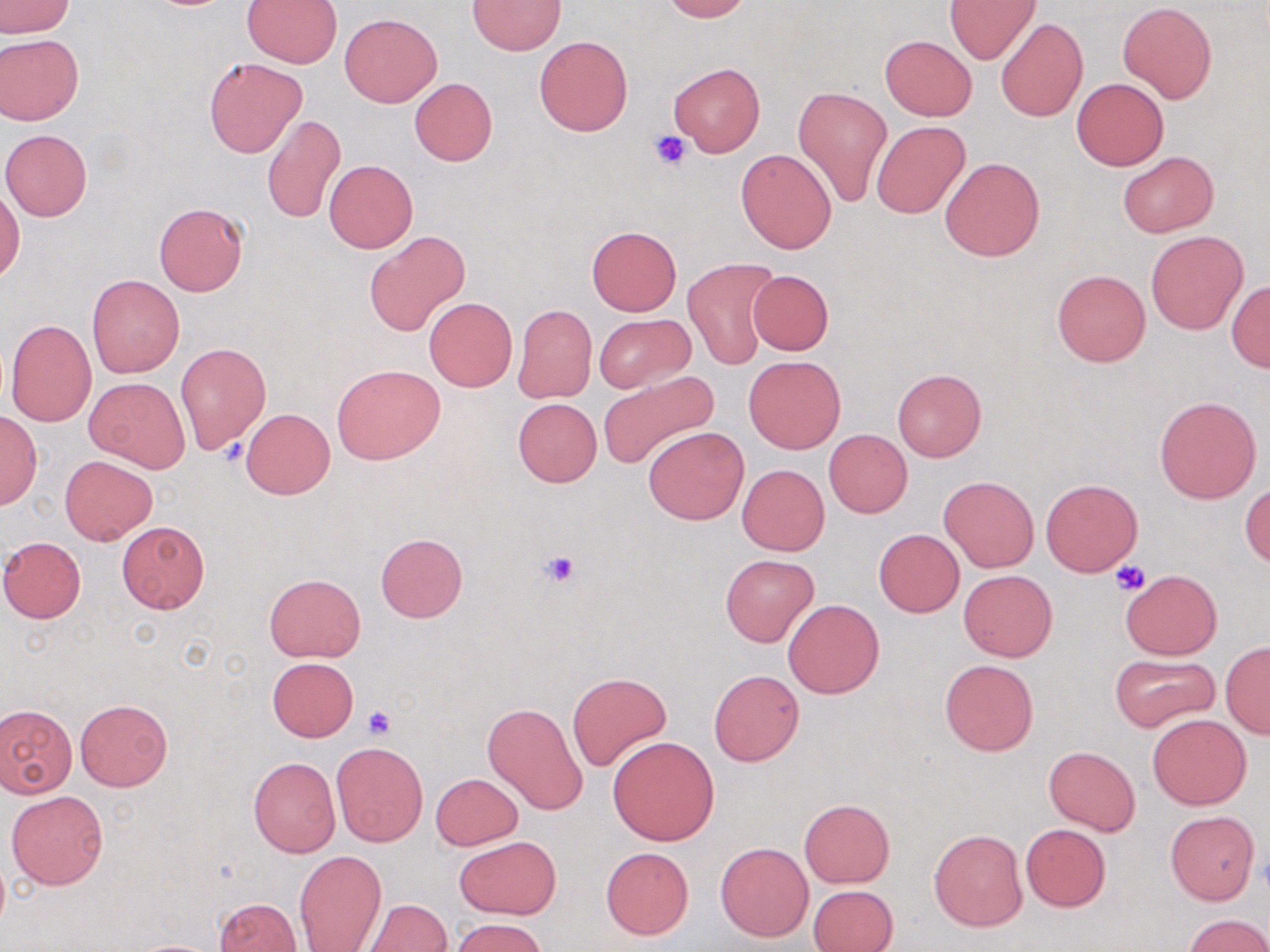

Approximate bounding boxes as [x1, y1, x2, y2] in pixels. Platelet locations: [650, 130, 690, 170], [542, 551, 579, 585], [1110, 562, 1150, 596], [361, 707, 396, 740]. Uninfected red blood cell locations: [0, 0, 74, 38], [659, 0, 751, 22], [945, 0, 1039, 65], [242, 1, 344, 67], [469, 1, 565, 54], [1117, 2, 1215, 103], [340, 13, 441, 106], [995, 18, 1088, 122], [0, 34, 83, 127], [879, 35, 977, 120], [535, 36, 632, 136], [203, 57, 306, 157], [670, 63, 764, 156], [409, 78, 497, 166], [1072, 78, 1168, 170], [794, 86, 891, 210], [261, 114, 345, 225], [871, 120, 970, 219], [1, 129, 92, 221], [736, 148, 837, 254], [1117, 150, 1219, 238], [939, 156, 1045, 262], [324, 160, 416, 253], [1, 186, 23, 284], [154, 202, 248, 296], [587, 225, 681, 316], [365, 230, 468, 336], [1146, 232, 1247, 334], [682, 259, 775, 370], [1052, 269, 1150, 367], [746, 270, 834, 356], [86, 273, 185, 378], [1226, 279, 1270, 372], [423, 298, 518, 391], [513, 304, 597, 403], [594, 313, 693, 393], [5, 318, 97, 427], [174, 341, 271, 455], [744, 356, 845, 454], [331, 363, 445, 463], [893, 368, 986, 461], [598, 370, 721, 471], [85, 376, 189, 472], [1154, 395, 1262, 504], [513, 398, 602, 487], [242, 409, 335, 499], [0, 410, 40, 509], [643, 427, 748, 524], [824, 430, 912, 517], [60, 456, 156, 544], [737, 463, 829, 555], [940, 476, 1039, 573], [1040, 478, 1142, 576], [1241, 482, 1269, 568], [117, 520, 210, 613], [873, 528, 965, 618], [376, 533, 468, 622], [0, 536, 87, 623], [721, 555, 818, 646], [1121, 569, 1222, 660], [958, 570, 1059, 662], [264, 573, 366, 661], [783, 599, 884, 698], [1220, 643, 1270, 738], [1109, 653, 1219, 733], [267, 658, 359, 741], [940, 659, 1038, 756], [709, 669, 805, 765], [567, 672, 671, 772], [75, 698, 172, 790], [482, 702, 589, 814], [0, 703, 77, 798], [582, 703, 696, 828], [1148, 714, 1251, 810], [607, 736, 720, 845], [330, 742, 429, 848], [1044, 747, 1140, 835], [248, 757, 340, 857], [431, 773, 523, 850], [7, 789, 109, 889], [799, 798, 894, 888], [1165, 812, 1259, 904], [1020, 824, 1111, 911], [928, 828, 1026, 931], [454, 836, 560, 918], [716, 842, 813, 942], [601, 847, 693, 940], [294, 849, 387, 951], [808, 884, 898, 952], [214, 897, 301, 951], [365, 898, 451, 951], [1182, 914, 1270, 952], [452, 917, 549, 952], [126, 939, 227, 952]. Slide-level diagnosis: no evidence of blood parasites. May-Grünwald-Giemsa stain. Single field of view. Captured at 1000x magnification. Image is 1270×952 pixels. Optical microscopy. Thin blood film.